Report the malaria status of this cell.
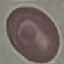

Uninfected.

Thin blood smear. Automatically extracted cell patch, resized to 64 × 64 pixels. Acquired by smartphone through the microscope eyepiece. Giemsa stain.